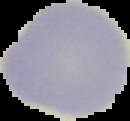
result = no malaria parasites seen
preparation = thin blood film
image type = segmented cell region on a black background
image size = 130×121 pixels